State which cell type is depicted.
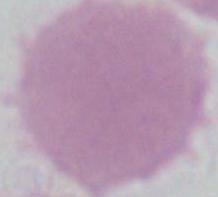

An erythrocyte.

Photomicrograph. 1000x magnification.